Give the preparation type.
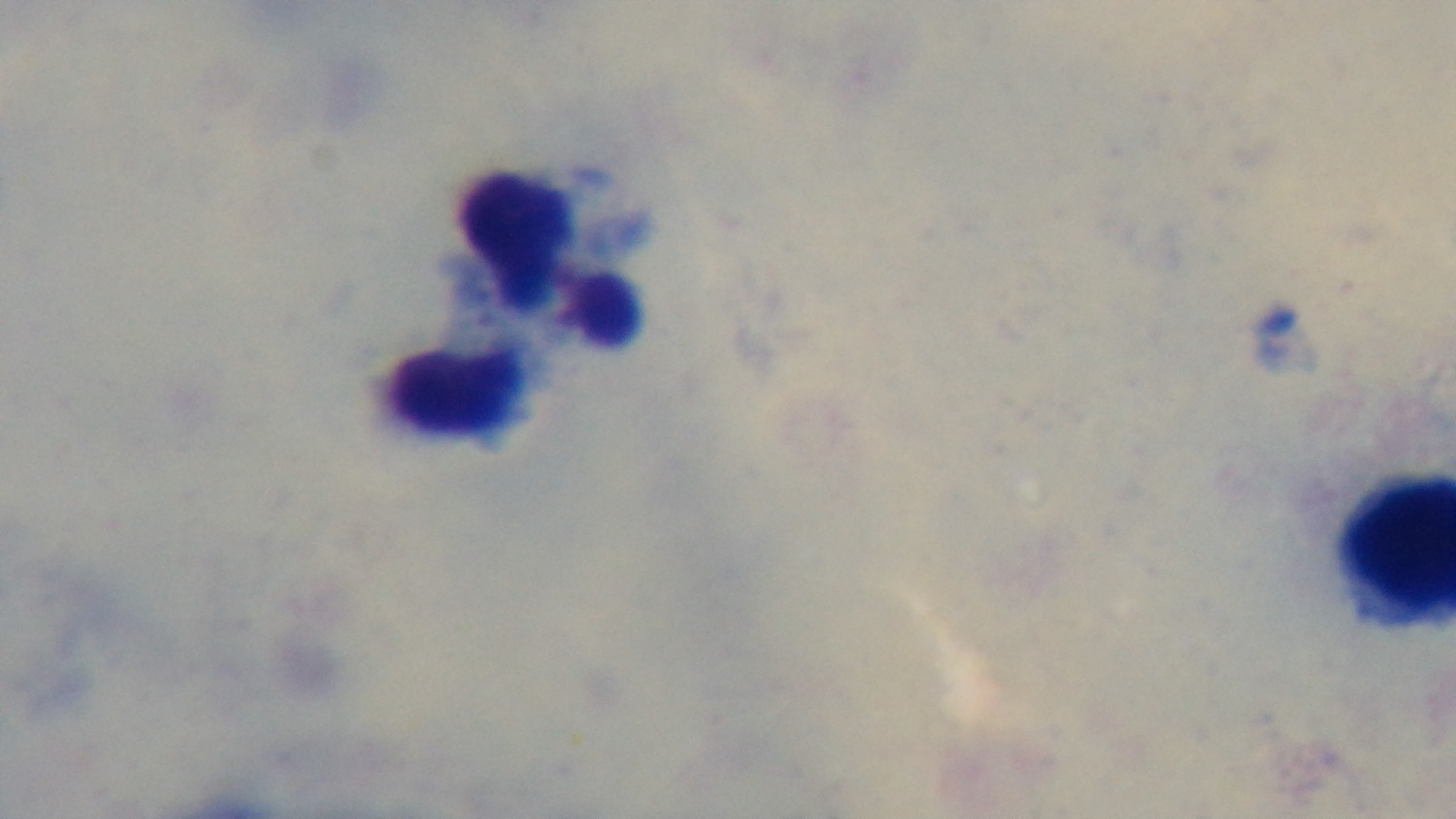

It is a thick blood film.

Light microscopy. Oil-immersion objective, 100x. Malaria status: negative. Giemsa-stained. Single field of view. Captured with a mounted 4K digital camera.